Assess this cell for malaria.
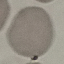

It is uninfected.

Giemsa stain. Automatically extracted cell patch, resized to 64 × 64 pixels. Thin smear of blood. Acquired by smartphone through the microscope eyepiece.